Locate every Plasmodium parasite and every leukocyte.
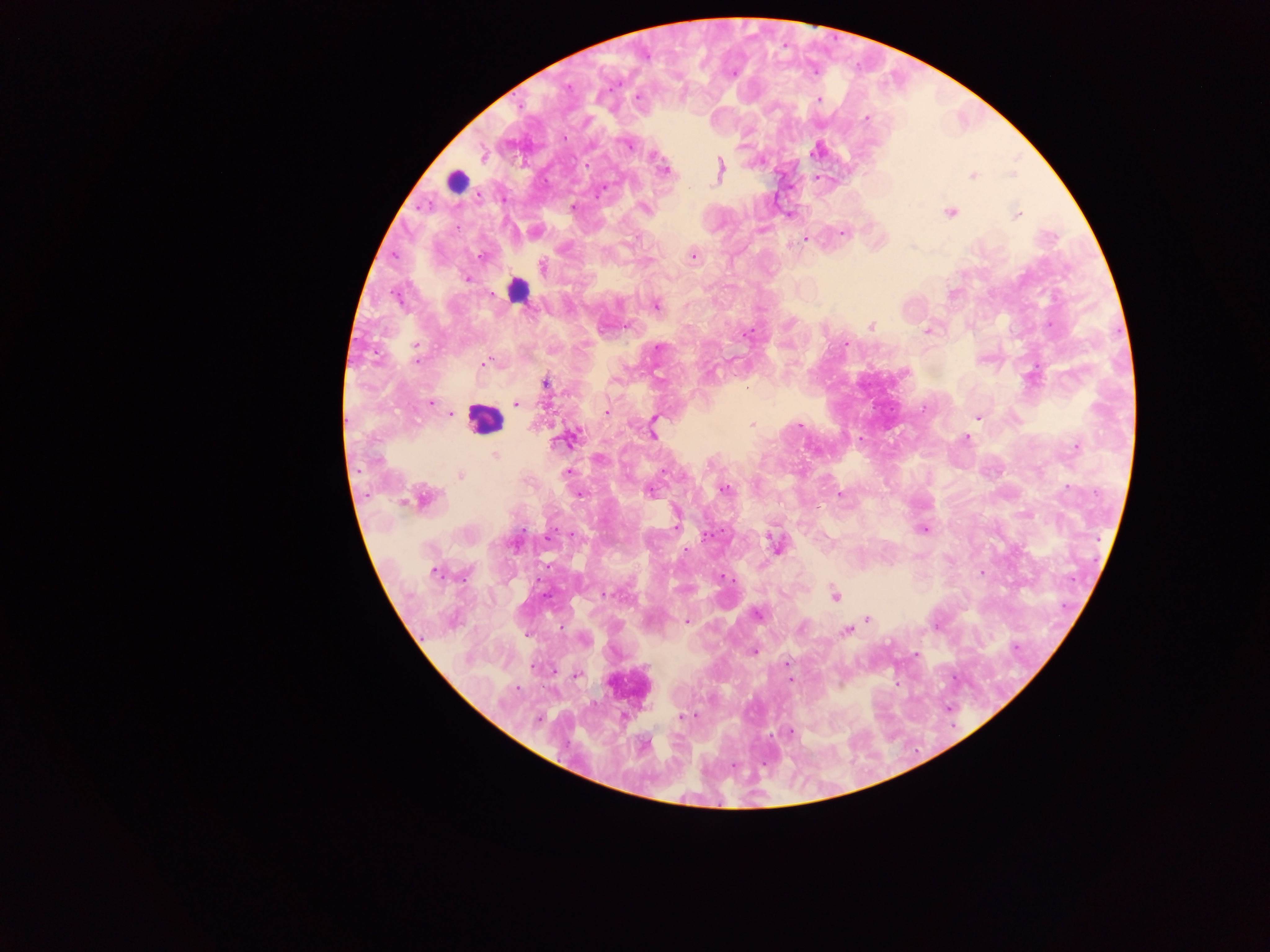
Approximate centers as x y in pixels.
Plasmodium parasites: 567 87; 638 97; 819 100; 866 118; 628 144; 484 156; 587 165; 720 169; 664 170; 972 176; 573 206; 644 208; 950 213; 1016 215; 842 232; 805 240; 693 256; 480 257; 543 268; 467 279; 656 305; 871 326; 927 332; 746 334; 845 344; 416 348; 658 348; 416 360; 485 363; 546 383; 430 403; 516 403; 606 412; 451 414; 978 417; 752 425; 800 426; 652 435; 570 438; 966 438; 860 440; 1076 447; 495 454; 567 473; 460 476; 725 490; 650 492; 840 493; 580 494; 425 499; 677 525; 923 529; 707 536; 549 537; 774 543; 686 550; 435 572; 981 573; 721 577; 608 595; 835 595; 758 614; 868 618; 686 620; 562 628; 802 628; 846 631; 754 651; 916 655; 787 663; 578 674; 790 679; 517 689; 682 716; 790 731.
Leukocytes: 456 182; 517 290; 484 418; 630 687.

capture = mobile-phone photograph through a microscope
image size = 1270×952 pixels
country = Ghana
preparation = thick blood film
field of view = single